Report the malaria status of this cell.
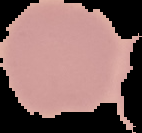

It is uninfected.

Image is 142×133 pixels. Segmented cell region on a black background. From a thin blood film.